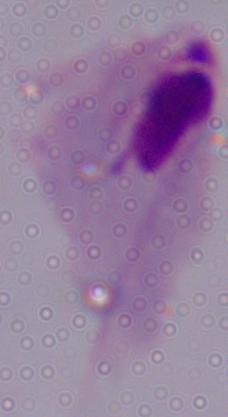
modality = photomicrograph
identification = trichomonad
magnification = 1000x